Identify the cell.
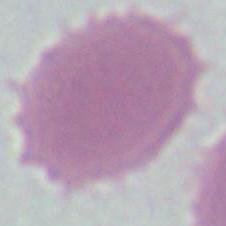

This is an erythrocyte.

{
  "modality": "micrograph",
  "magnification": "1000x"
}